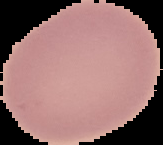
image type = segmented cell region on a black background
image size = 163×145 pixels
malaria status = uninfected
preparation = thin blood film